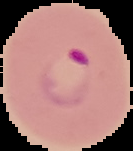 Malaria status: parasitized. Image is 133×151 pixels. From a thin blood film. The area outside the segmented cell region is set to black.